Identify the preparation type.
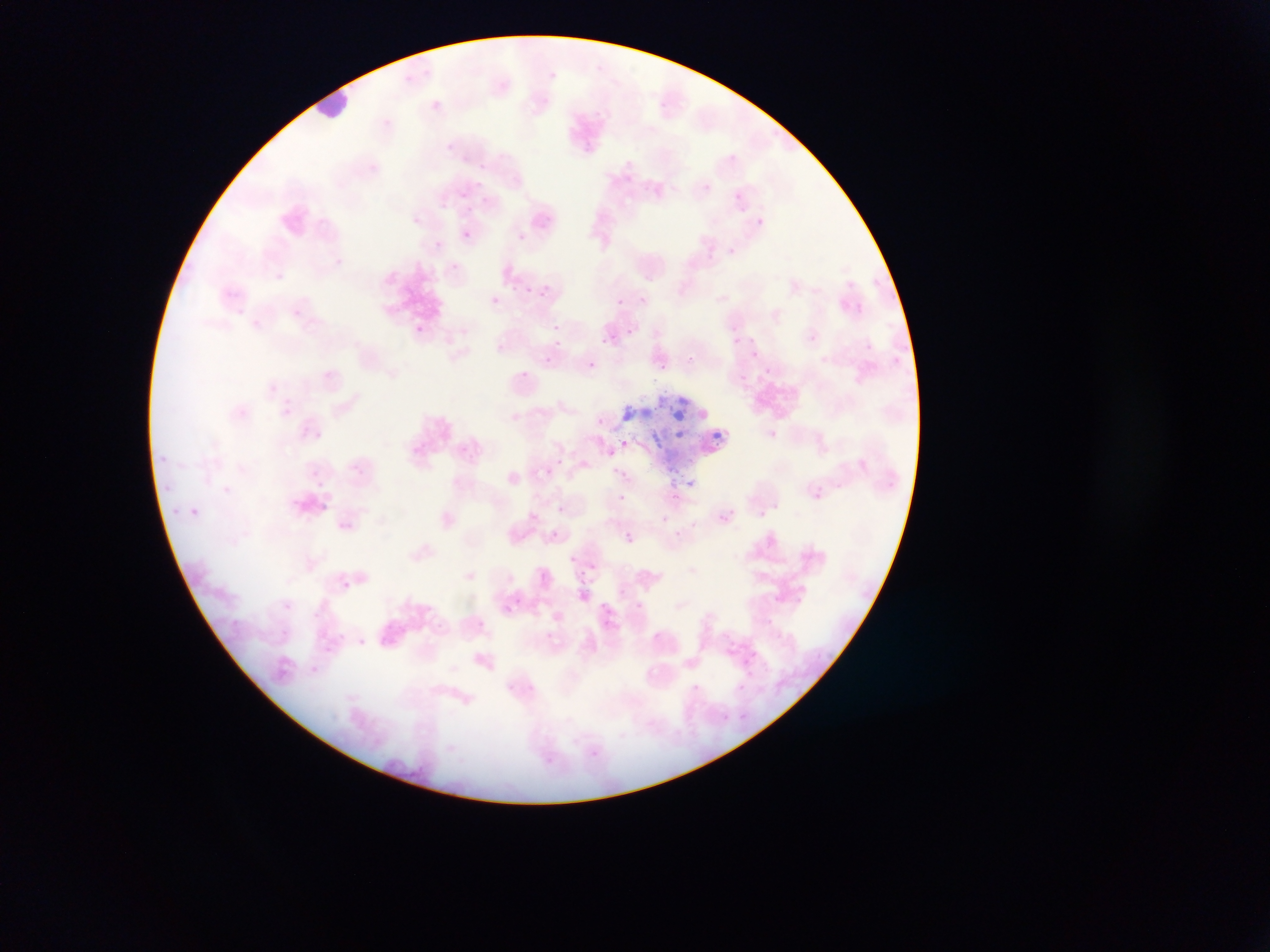

This is a thin smear.

Approximate bounding boxes as {left, top, right, bottom} in pixels. Plasmodium parasite locations: {428, 99, 442, 112}, {580, 142, 594, 155}, {445, 143, 454, 152}, {460, 190, 470, 199}, {731, 190, 745, 205}, {755, 217, 764, 226}, {461, 230, 471, 240}, {517, 233, 526, 242}, {433, 241, 442, 250}, {449, 264, 460, 275}, {524, 286, 534, 295}, {539, 287, 549, 303}, {489, 295, 501, 306}, {638, 296, 647, 304}, {616, 299, 624, 307}, {855, 304, 863, 312}, {551, 323, 561, 333}, {621, 323, 633, 339}, {730, 323, 739, 333}, {414, 324, 423, 333}, {600, 329, 612, 349}, {807, 334, 818, 344}, {747, 335, 758, 346}, {554, 338, 567, 349}, {542, 347, 556, 363}, {749, 349, 758, 359}, {685, 350, 693, 365}, {586, 357, 597, 377}, {659, 358, 666, 372}, {763, 367, 771, 375}, {516, 369, 531, 383}, {596, 416, 605, 425}, {768, 430, 778, 439}, {620, 439, 630, 448}, {349, 462, 361, 473}, {542, 467, 553, 477}, {310, 469, 321, 479}, {684, 478, 695, 489}, {811, 488, 823, 499}, {669, 491, 683, 504}, {617, 493, 627, 502}, {555, 504, 566, 513}, {759, 505, 773, 517}, {187, 506, 201, 519}, {758, 509, 768, 519}, {717, 510, 734, 524}, {660, 514, 670, 524}, {549, 528, 561, 540}, {624, 533, 634, 543}, {568, 556, 576, 563}, {588, 564, 596, 572}, {537, 569, 549, 581}, {340, 579, 351, 590}, {618, 587, 626, 596}, {579, 590, 589, 601}, {283, 602, 293, 611}, {635, 603, 644, 610}, {600, 604, 611, 613}, {475, 618, 485, 628}, {279, 629, 290, 639}, {735, 683, 745, 692}, {691, 684, 700, 692}, {721, 714, 731, 723}. Leukocyte locations: {315, 82, 354, 139}. Artifact (stain precipitate or debris) locations: {624, 394, 736, 468}. Mobile-phone photograph taken through the microscope. One field of view. Sample from Ghana. Image is 1270×952 pixels.